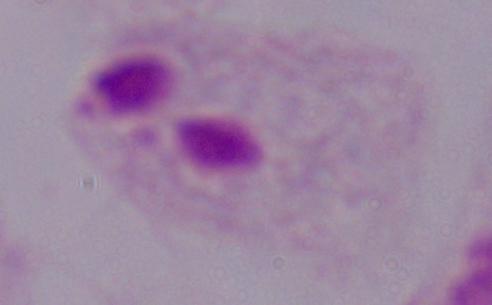 A trichomonad is seen. Captured at 1000x magnification. Micrograph.